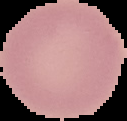

Malaria status: uninfected. From a thin blood film. Image is 127×121 pixels. Cell region segmented out of the field of view; the surrounding area is masked to black.